Locate and identify every blood parasite.
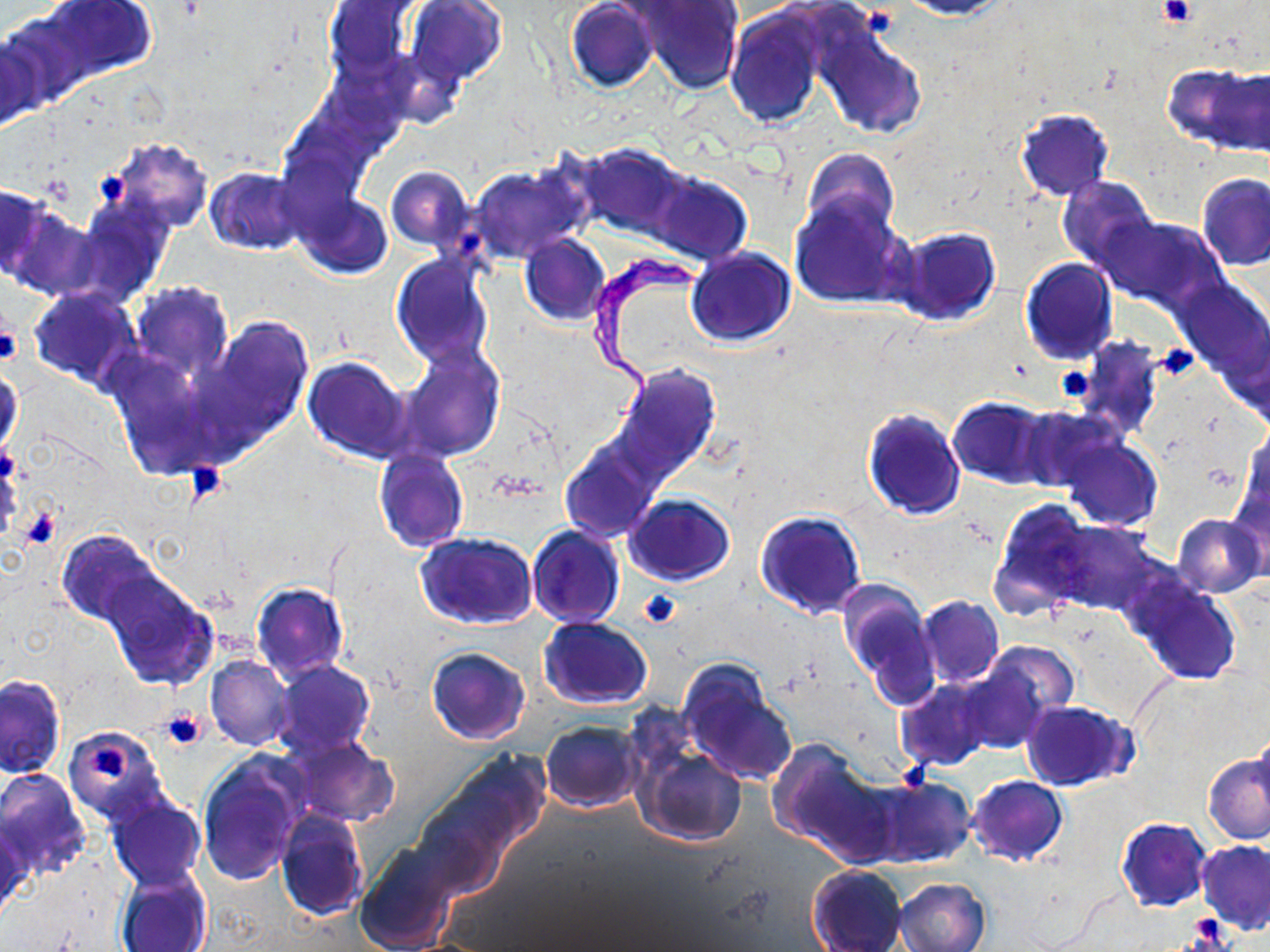
Approximate bounding boxes as (x1,y1)-(x2,y2) corner pairs in pixels.
Trypanosoma brucei: (589,251)-(715,430).
No Plasmodium falciparum, Plasmodium ovale, Plasmodium malariae, Plasmodium vivax, or Babesia divergens observed.

Uninfected red blood cell locations: (40,0)-(157,82), (565,0)-(659,92), (900,0)-(1014,20), (325,1)-(415,78), (406,1)-(505,85), (636,1)-(743,94), (0,9)-(93,111), (725,9)-(827,128), (814,21)-(927,141), (0,29)-(43,136), (1167,64)-(1264,151), (1014,108)-(1114,201), (104,139)-(213,234), (575,142)-(692,242), (802,148)-(899,240), (467,162)-(591,262), (387,166)-(475,252), (205,167)-(306,255), (649,171)-(752,265), (1198,174)-(1270,271), (1056,175)-(1159,270), (0,184)-(49,282), (296,194)-(393,279), (789,196)-(912,310), (70,200)-(172,306), (7,205)-(99,300), (1097,214)-(1227,314), (892,226)-(1001,325), (519,234)-(610,326), (685,247)-(795,347), (391,254)-(494,368), (1020,257)-(1118,364), (1173,278)-(1270,383), (128,281)-(232,381), (28,288)-(139,386), (208,318)-(313,438), (1222,324)-(1270,428), (1073,340)-(1165,439), (402,350)-(503,460), (304,357)-(412,461), (616,364)-(721,478), (0,365)-(21,458), (948,398)-(1051,487), (1017,405)-(1123,492), (862,408)-(966,521), (1058,433)-(1163,531), (559,443)-(659,542), (374,451)-(469,552), (625,494)-(734,586), (989,500)-(1092,619), (756,510)-(868,618), (1172,513)-(1266,596), (1049,521)-(1155,614), (528,525)-(624,627), (55,529)-(161,628), (416,532)-(540,631), (99,570)-(218,691), (1127,578)-(1243,685), (838,581)-(939,699), (251,584)-(348,681), (917,596)-(1003,687), (538,616)-(653,708), (981,641)-(1079,732), (424,646)-(532,745), (206,656)-(292,750), (272,660)-(376,762), (954,660)-(1052,754), (676,661)-(798,787), (0,674)-(65,778), (895,677)-(996,772), (1021,700)-(1135,792), (540,721)-(644,812), (60,726)-(171,829), (1252,729)-(1270,818), (288,738)-(399,828), (769,742)-(883,858), (637,746)-(747,847), (413,751)-(552,896), (1203,753)-(1270,845), (198,759)-(302,886), (0,769)-(91,879), (967,775)-(1068,866), (866,776)-(975,868), (107,796)-(206,890), (276,808)-(367,920), (0,817)-(29,922), (1116,818)-(1211,912), (1198,840)-(1270,934), (355,847)-(456,952), (807,864)-(908,951), (115,869)-(211,952), (894,877)-(990,952). Platelet locations: (1159,0)-(1196,28), (94,166)-(136,210), (0,312)-(22,367), (1155,342)-(1201,381), (1054,366)-(1094,403), (182,459)-(233,506), (17,505)-(63,552), (638,589)-(681,628), (159,709)-(206,752), (90,744)-(133,782), (1186,917)-(1235,947). Slide-level diagnosis: Trypanosoma brucei. One field of a larger specimen. Captured at 1000x magnification. Light microscopy. Image is 1270×952 pixels. Thin blood smear. May-Grünwald-Giemsa stain.